Outline each blood parasite and name the species.
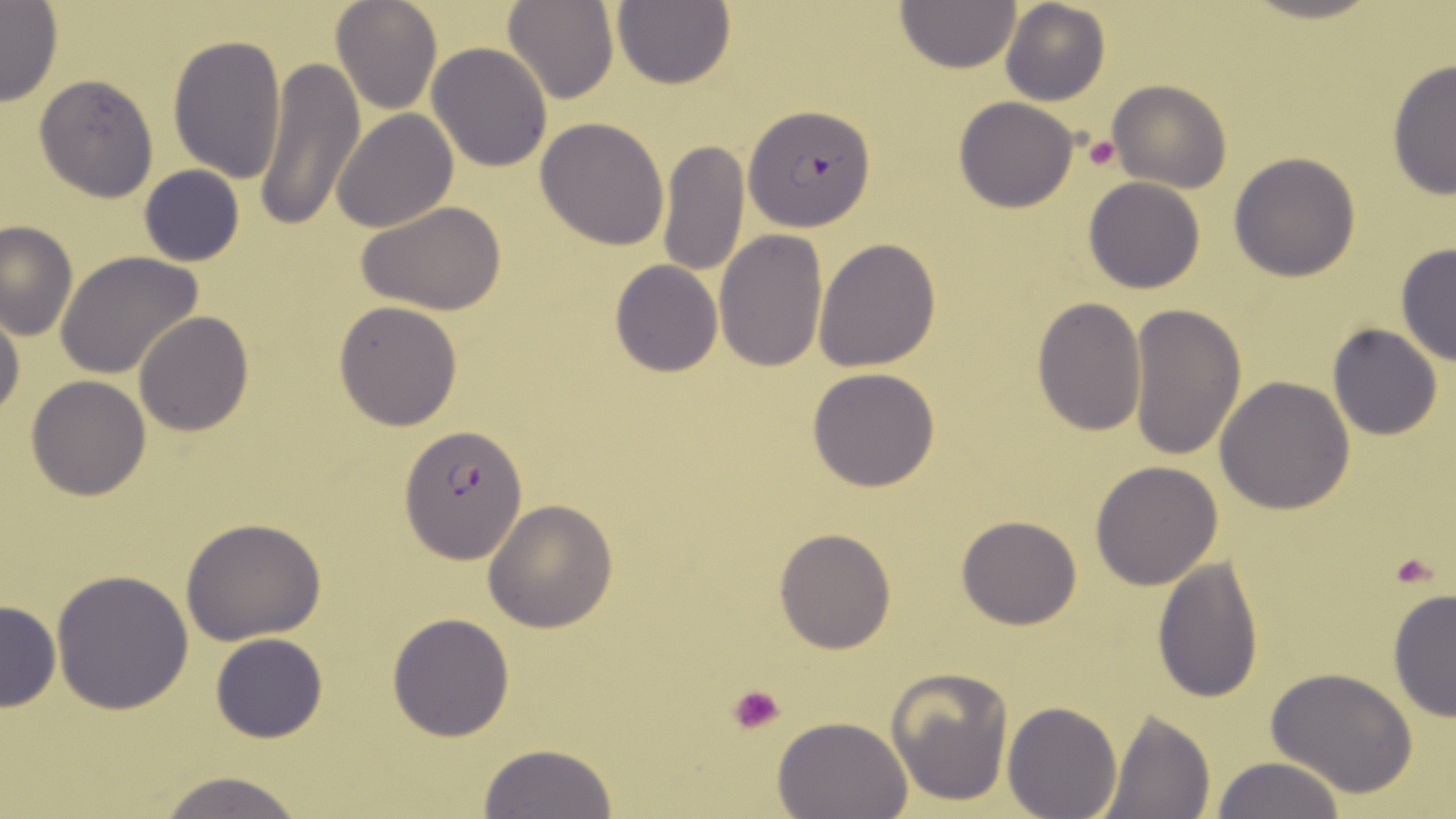
Approximate bounding boxes as (x1, y1, x2, y2) in pixels.
Plasmodium falciparum-infected red blood cells: (744, 105, 875, 231), (402, 424, 526, 565).
No Plasmodium ovale, Plasmodium malariae, Plasmodium vivax, Babesia divergens, or Trypanosoma brucei observed.

{
  "slide_level_diagnosis": "Plasmodium falciparum",
  "platelet_locations": "approximate bounding boxes as (x1, y1, x2, y2) in pixels: (1082, 132, 1122, 173), (1394, 558, 1434, 589), (728, 684, 788, 734)",
  "field_of_view": "single",
  "modality": "optical microscopy",
  "magnification": "1000x",
  "image_size": "1456×819 pixels",
  "preparation": "thin blood smear",
  "uninfected_red_blood_cell_locations": "approximate bounding boxes as (x1, y1, x2, y2) in pixels: (502, 0, 617, 105), (1000, 0, 1111, 106), (330, 1, 441, 114), (896, 1, 1020, 73), (611, 2, 735, 89), (0, 3, 62, 105), (167, 31, 287, 185), (427, 42, 553, 172), (252, 57, 364, 231), (1387, 57, 1455, 200), (34, 74, 160, 201), (1107, 79, 1231, 193), (953, 96, 1080, 212), (332, 108, 458, 231), (537, 116, 670, 249), (657, 139, 749, 278), (1229, 151, 1362, 282), (139, 166, 245, 265), (1083, 176, 1204, 293), (357, 201, 506, 315), (0, 219, 78, 340), (715, 230, 828, 373), (814, 237, 942, 372), (1394, 243, 1456, 367), (55, 251, 204, 378), (609, 260, 723, 376), (1030, 296, 1146, 435), (333, 300, 463, 431), (1130, 301, 1246, 463), (0, 306, 23, 419), (133, 311, 253, 436), (1328, 323, 1443, 440), (807, 367, 940, 492), (1214, 375, 1356, 515), (26, 376, 152, 501), (1090, 461, 1225, 590), (484, 498, 618, 631), (955, 516, 1081, 630), (182, 517, 328, 646), (773, 526, 897, 654), (1152, 554, 1264, 704), (51, 569, 194, 714), (1388, 587, 1456, 724), (0, 598, 60, 713), (387, 612, 514, 740), (210, 633, 327, 743), (1265, 667, 1420, 799), (886, 668, 1014, 807), (1003, 701, 1121, 818), (1099, 708, 1216, 819), (772, 715, 915, 819), (477, 743, 619, 819), (1211, 755, 1348, 818), (151, 771, 308, 819)",
  "stain": "May-Grünwald-Giemsa"
}